Locate every Plasmodium malariae-infected red blood cell.
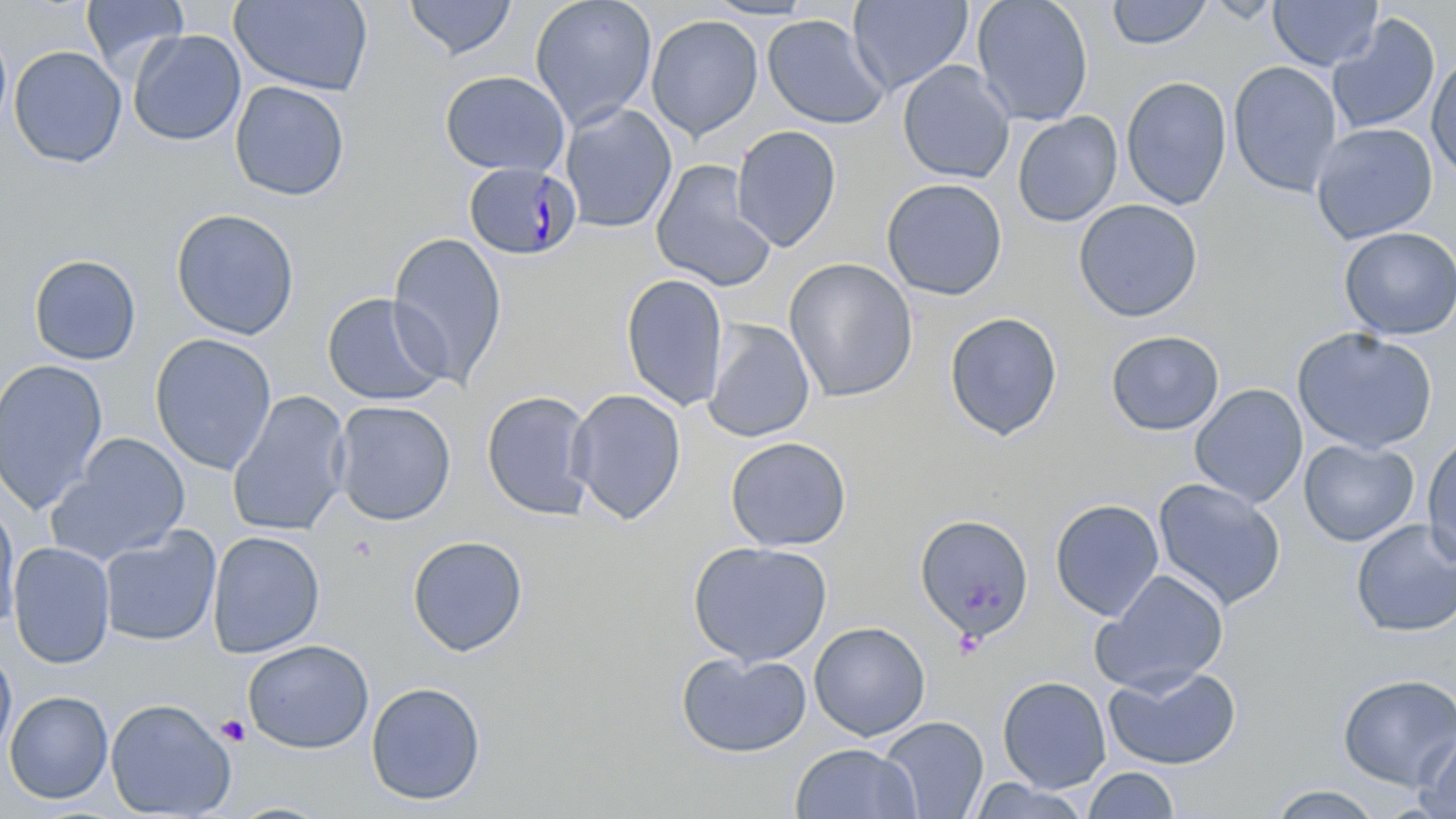

Approximate bounding boxes as [x1, y1, x2, y2] in pixels.
Plasmodium malariae-infected red blood cells: [463, 162, 581, 261].

{
  "slide_level_diagnosis": "Plasmodium malariae",
  "preparation": "thin blood film",
  "magnification": "1000x",
  "platelet_locations": "approximate bounding boxes as [x1, y1, x2, y2] in pixels: [346, 535, 378, 563], [215, 715, 251, 746]",
  "image_size": "1456×819 pixels",
  "modality": "light microscopy",
  "field_of_view": "single",
  "stain": "May-Grünwald-Giemsa",
  "uninfected_red_blood_cell_locations": "approximate bounding boxes as [x1, y1, x2, y2] in pixels: [81, 0, 188, 75], [230, 0, 373, 96], [403, 0, 517, 60], [529, 0, 657, 129], [701, 0, 819, 20], [849, 0, 974, 96], [971, 0, 1094, 127], [1106, 0, 1213, 49], [1268, 0, 1382, 71], [645, 14, 763, 140], [761, 14, 889, 130], [1327, 14, 1440, 136], [0, 26, 12, 139], [127, 29, 247, 146], [8, 45, 127, 168], [1426, 55, 1456, 182], [1227, 60, 1343, 197], [896, 61, 1015, 183], [439, 69, 571, 177], [1120, 76, 1233, 210], [229, 80, 350, 201], [559, 103, 677, 233], [1012, 111, 1123, 227], [1310, 122, 1438, 244], [731, 125, 842, 252], [650, 159, 776, 291], [881, 178, 1008, 300], [1073, 198, 1203, 322], [171, 208, 300, 340], [1338, 226, 1456, 340], [386, 232, 507, 388], [28, 254, 142, 365], [783, 257, 919, 403], [621, 273, 729, 411], [321, 292, 450, 407], [944, 311, 1063, 441], [702, 319, 815, 443], [1292, 327, 1438, 454], [1106, 330, 1224, 436], [149, 333, 277, 475], [0, 359, 109, 515], [1189, 383, 1308, 508], [567, 388, 686, 524], [480, 389, 596, 521], [226, 390, 351, 537], [331, 400, 456, 526], [1422, 432, 1456, 568], [50, 433, 192, 564], [724, 436, 852, 552], [1299, 438, 1419, 546], [1152, 477, 1287, 611], [0, 498, 21, 635], [1049, 498, 1165, 621], [915, 513, 1034, 641], [1350, 518, 1456, 637], [99, 526, 221, 646], [207, 530, 325, 658], [407, 534, 529, 656], [688, 540, 833, 667], [8, 541, 115, 669], [1092, 569, 1229, 695], [809, 621, 930, 740], [242, 639, 374, 754], [0, 645, 17, 760], [676, 651, 812, 758], [1104, 665, 1242, 770], [1337, 673, 1456, 790], [997, 675, 1112, 793], [365, 681, 486, 806], [4, 690, 113, 804], [105, 697, 237, 818], [878, 716, 988, 818], [1415, 729, 1456, 819], [790, 742, 922, 819], [1082, 766, 1180, 819], [967, 779, 1093, 818], [1266, 784, 1384, 819]"
}